Identify the parasite.
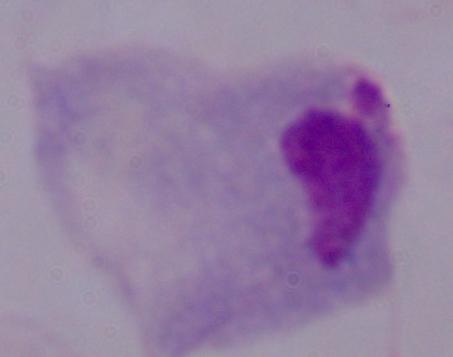
A trichomonad.

Photomicrograph. 1000x magnification.